Classify this cell by malaria status.
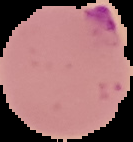
Parasitized.

preparation = thin blood smear
image size = 133×142 pixels
image type = segmented cell region with the area outside set to black